Comment on the morphology of the red blood cells.
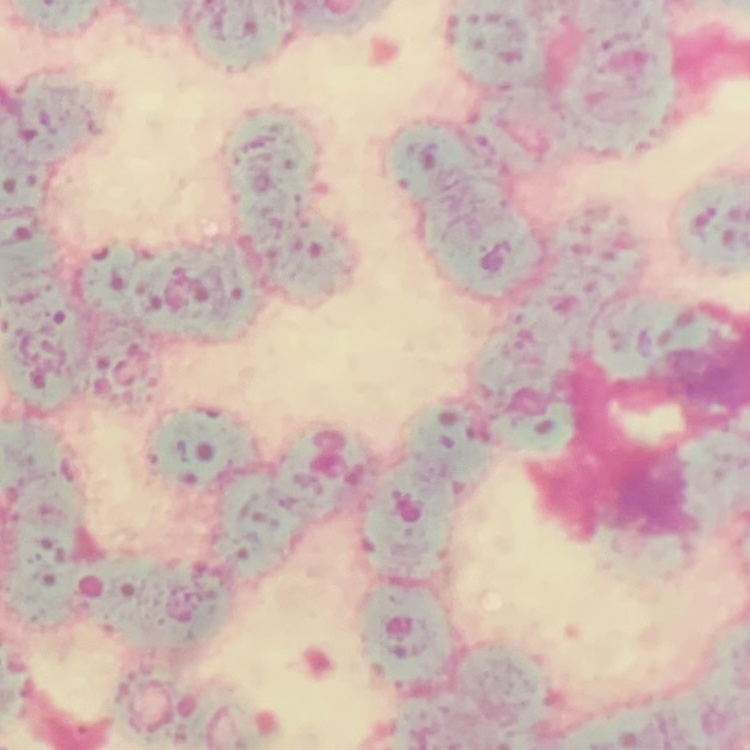

Rouleaux formation.

Summary:
  - Preparation: thin peripheral smear
  - Stain: Field's or Giemsa
  - Image type: one tile cut from a larger photomicrograph